Give the position of every leukocyte visible.
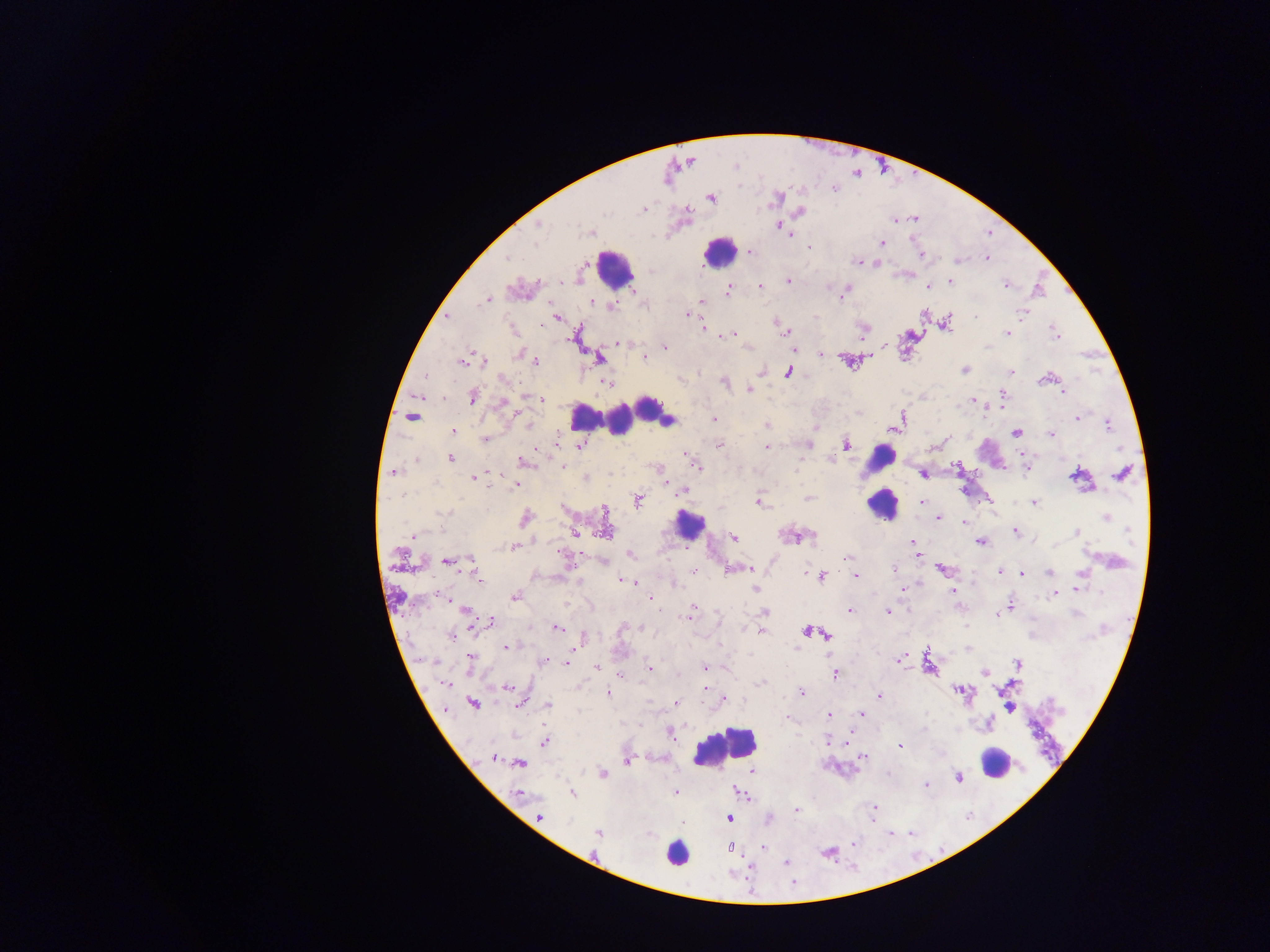
Approximate centers as (x, y) in pixels.
Leukocytes: (718, 251), (614, 267), (647, 407), (583, 415), (671, 420), (618, 421), (880, 459), (881, 505), (689, 524), (724, 747), (995, 762), (676, 852).

plasmodium_parasite_locations: 'approximate centers as (x, y) in pixels: (736, 166), (711, 197), (776, 198), (644, 209), (800, 212), (894, 221), (538, 225), (781, 227), (589, 232), (883, 242), (808, 247), (750, 252), (921, 256), (508, 258), (987, 258), (957, 260), (858, 262), (876, 264), (788, 280), (950, 282), (1005, 285), (759, 286), (927, 286), (633, 289), (728, 290), (842, 293), (487, 300), (703, 301), (592, 302), (611, 306), (1022, 313), (687, 314), (924, 315), (976, 317), (555, 318), (948, 321), (511, 328), (703, 328), (863, 329), (785, 332), (1055, 332), (1007, 333), (730, 334), (619, 343), (885, 346), (665, 347), (988, 347), (520, 354), (822, 354), (870, 356), (529, 357), (644, 357), (599, 358), (483, 360), (535, 360), (463, 361), (964, 369), (1011, 371), (788, 372), (504, 379), (1042, 380), (725, 382), (607, 383), (750, 389), (1062, 392), (1003, 394), (534, 396), (473, 397), (541, 399), (973, 399), (503, 402), (412, 417), (901, 417), (1077, 417), (714, 419), (528, 424), (1108, 424), (766, 426), (894, 429), (454, 430), (1016, 433), (1051, 435), (484, 439), (720, 444), (808, 445), (846, 445), (580, 446), (766, 447), (687, 454), (1023, 455), (450, 459), (691, 459), (829, 459), (417, 460), (524, 462), (562, 465), (957, 465), (697, 467), (1027, 470), (393, 472), (1122, 473), (923, 474), (1074, 475), (482, 477), (474, 478), (586, 478), (515, 486), (682, 491), (809, 498), (638, 500), (758, 501), (922, 502), (1034, 503), (443, 513), (1106, 517), (937, 518), (525, 519), (964, 522), (1015, 530), (606, 531), (1077, 532), (575, 533), (412, 535), (810, 535), (733, 536), (792, 536), (913, 542), (981, 542), (513, 547), (914, 547), (562, 555), (632, 555), (917, 555), (847, 557), (447, 562), (473, 568), (747, 568), (893, 568), (731, 569), (942, 570), (694, 572), (998, 572), (1021, 573), (1049, 573), (805, 574), (477, 576), (855, 576), (822, 577), (622, 580), (633, 582), (755, 589), (902, 589), (1077, 589), (953, 591), (1100, 592), (1054, 593), (515, 596), (650, 599), (1012, 605), (464, 609), (692, 610), (850, 610), (765, 611), (887, 612), (997, 616), (688, 617), (491, 622), (557, 628), (644, 628), (761, 632), (806, 632), (451, 635), (827, 635), (585, 637), (506, 647), (470, 659), (900, 659), (544, 660), (568, 662), (1018, 662), (597, 667), (650, 668), (705, 668), (984, 673), (835, 674), (621, 677), (761, 682), (446, 684), (507, 687), (705, 688), (961, 691), (801, 692), (608, 694), (879, 696), (724, 699), (472, 704), (548, 704), (676, 704), (518, 705), (862, 714), (829, 715), (787, 718), (671, 734), (545, 741), (829, 742), (900, 746), (863, 757), (494, 758), (627, 762), (520, 764), (752, 770), (602, 774), (888, 774), (956, 777), (925, 785), (676, 792), (740, 793), (519, 794), (573, 794), (874, 807), (796, 810), (539, 817), (729, 819), (682, 822), (598, 833), (729, 848), (764, 848), (785, 863)'
image_size: 1270×952 pixels
capture: mobile-phone photograph through a microscope
field_of_view: single
country: Ghana
preparation: thick blood smear